Outline each blood parasite and name the species.
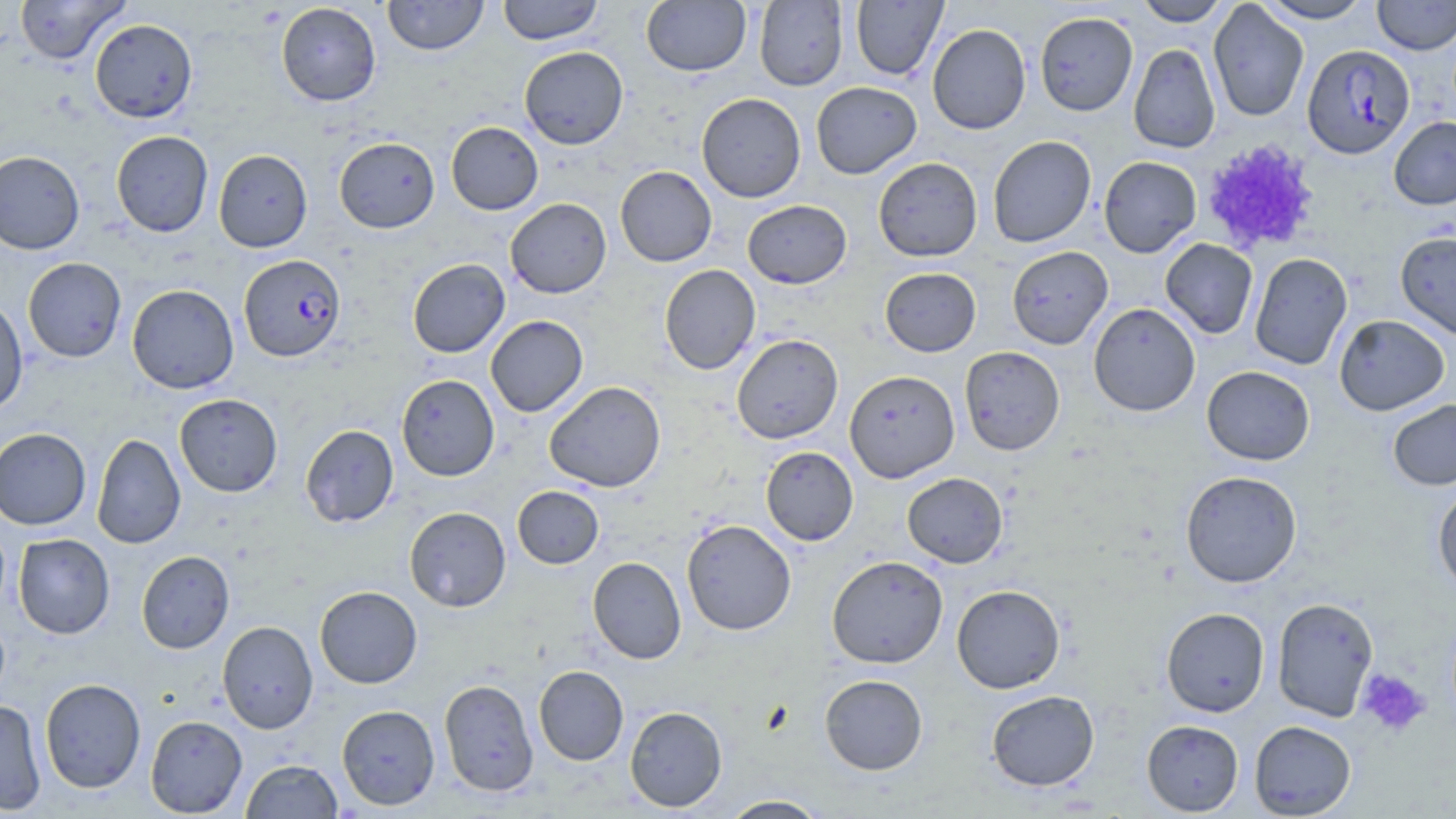

Approximate bounding boxes as named x1/y1/x2/y2 corners in pixels.
Plasmodium falciparum-infected red blood cells: (x1=1302, y1=44, x2=1415, y2=159), (x1=239, y1=255, x2=346, y2=362).
No Plasmodium ovale, Plasmodium malariae, Plasmodium vivax, Babesia divergens, or Trypanosoma brucei observed.

{
  "slide_level_diagnosis": "Plasmodium falciparum",
  "uninfected_red_blood_cell_locations": "approximate bounding boxes as named x1/y1/x2/y2 corners in pixels: (x1=14, y1=0, x2=129, y2=64), (x1=382, y1=0, x2=489, y2=56), (x1=497, y1=0, x2=604, y2=45), (x1=851, y1=0, x2=947, y2=80), (x1=1134, y1=0, x2=1232, y2=26), (x1=1256, y1=0, x2=1374, y2=23), (x1=1373, y1=0, x2=1456, y2=55), (x1=641, y1=1, x2=751, y2=76), (x1=755, y1=1, x2=848, y2=91), (x1=1208, y1=1, x2=1309, y2=122), (x1=276, y1=2, x2=381, y2=106), (x1=1034, y1=11, x2=1138, y2=116), (x1=90, y1=19, x2=197, y2=123), (x1=927, y1=24, x2=1031, y2=135), (x1=1128, y1=43, x2=1220, y2=154), (x1=519, y1=46, x2=628, y2=149), (x1=811, y1=81, x2=922, y2=179), (x1=696, y1=93, x2=806, y2=202), (x1=1389, y1=116, x2=1456, y2=210), (x1=446, y1=122, x2=543, y2=215), (x1=111, y1=131, x2=213, y2=237), (x1=987, y1=135, x2=1096, y2=248), (x1=334, y1=137, x2=439, y2=233), (x1=213, y1=149, x2=312, y2=252), (x1=0, y1=151, x2=85, y2=255), (x1=1098, y1=156, x2=1202, y2=257), (x1=873, y1=157, x2=983, y2=261), (x1=615, y1=166, x2=717, y2=267), (x1=505, y1=198, x2=611, y2=298), (x1=742, y1=200, x2=852, y2=288), (x1=1396, y1=231, x2=1456, y2=341), (x1=1160, y1=238, x2=1258, y2=340), (x1=1006, y1=246, x2=1113, y2=349), (x1=1249, y1=252, x2=1353, y2=370), (x1=23, y1=257, x2=126, y2=362), (x1=407, y1=258, x2=510, y2=358), (x1=659, y1=264, x2=761, y2=374), (x1=880, y1=267, x2=981, y2=356), (x1=127, y1=284, x2=239, y2=394), (x1=0, y1=296, x2=28, y2=416), (x1=1088, y1=303, x2=1201, y2=416), (x1=1334, y1=314, x2=1449, y2=415), (x1=485, y1=315, x2=588, y2=417), (x1=731, y1=334, x2=843, y2=444), (x1=960, y1=346, x2=1065, y2=456), (x1=1202, y1=365, x2=1315, y2=465), (x1=845, y1=370, x2=960, y2=483), (x1=396, y1=374, x2=499, y2=481), (x1=544, y1=381, x2=666, y2=492), (x1=174, y1=393, x2=283, y2=497), (x1=1388, y1=399, x2=1456, y2=490), (x1=301, y1=424, x2=399, y2=528), (x1=0, y1=428, x2=91, y2=530), (x1=91, y1=432, x2=186, y2=549), (x1=760, y1=446, x2=858, y2=545), (x1=1180, y1=470, x2=1302, y2=587), (x1=902, y1=472, x2=1008, y2=568), (x1=512, y1=486, x2=603, y2=568), (x1=1433, y1=486, x2=1456, y2=595), (x1=404, y1=506, x2=511, y2=612), (x1=682, y1=519, x2=796, y2=635), (x1=13, y1=534, x2=114, y2=639), (x1=136, y1=551, x2=234, y2=654), (x1=826, y1=556, x2=948, y2=669), (x1=588, y1=557, x2=686, y2=663), (x1=952, y1=584, x2=1065, y2=693), (x1=314, y1=586, x2=422, y2=688), (x1=1271, y1=597, x2=1379, y2=722), (x1=1161, y1=607, x2=1270, y2=717), (x1=217, y1=621, x2=318, y2=734), (x1=533, y1=665, x2=629, y2=765), (x1=819, y1=674, x2=928, y2=774), (x1=40, y1=678, x2=146, y2=793), (x1=439, y1=679, x2=539, y2=796), (x1=986, y1=690, x2=1099, y2=791), (x1=0, y1=699, x2=46, y2=815), (x1=337, y1=704, x2=440, y2=810), (x1=624, y1=706, x2=727, y2=811), (x1=145, y1=715, x2=247, y2=817), (x1=1141, y1=719, x2=1244, y2=815), (x1=1249, y1=720, x2=1356, y2=818), (x1=241, y1=759, x2=342, y2=818), (x1=719, y1=795, x2=829, y2=818)",
  "image_size": "1456×819 pixels",
  "modality": "light microscopy",
  "stain": "May-Grünwald-Giemsa",
  "field_of_view": "single",
  "preparation": "thin blood film",
  "platelet_locations": "approximate bounding boxes as named x1/y1/x2/y2 corners in pixels: (x1=1201, y1=138, x2=1321, y2=254), (x1=1356, y1=668, x2=1430, y2=737)",
  "magnification": "1000x"
}